Report the malaria status of this cell.
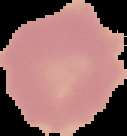
Uninfected.

Summary:
  - Image size: 127×136 pixels
  - Preparation: thin blood film
  - Image type: segmented cell region with the area outside set to black